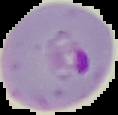 From a thin blood smear. Image is 118×115 pixels. Result: Plasmodium parasites detected. Segmented cell region on a black background.